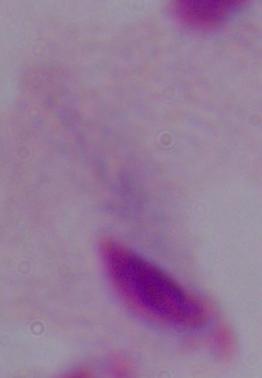
Summary:
  - Identification: trichomonad
  - Modality: micrograph
  - Magnification: 1000x